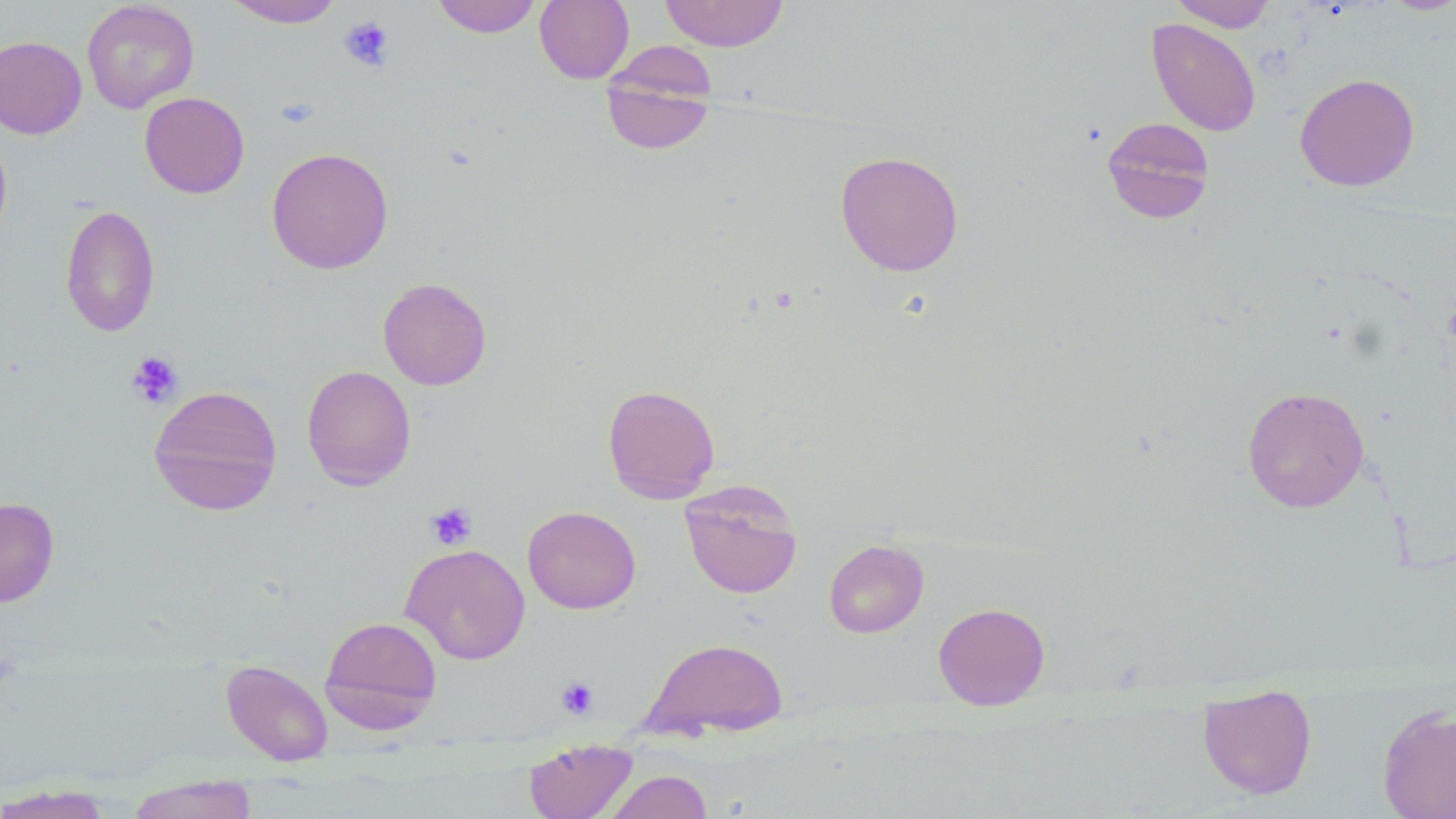
Approximate bounding boxes as (x1, y1, x2, y2) in pixels. Platelet locations: (338, 16, 394, 72), (276, 95, 318, 129), (126, 351, 183, 409), (425, 501, 478, 550), (555, 676, 599, 720). Uninfected red blood cell locations: (225, 0, 345, 28), (431, 0, 543, 38), (535, 0, 635, 84), (659, 0, 790, 52), (1169, 0, 1277, 32), (1379, 0, 1456, 16), (81, 1, 199, 113), (1147, 18, 1261, 137), (0, 36, 87, 139), (600, 42, 718, 155), (1294, 73, 1420, 192), (139, 92, 249, 198), (1101, 116, 1216, 224), (0, 128, 12, 245), (266, 147, 393, 274), (835, 150, 964, 276), (60, 204, 160, 337), (377, 277, 492, 390), (301, 365, 417, 491), (603, 384, 720, 504), (148, 385, 284, 516), (1241, 386, 1369, 513), (679, 481, 803, 599), (0, 497, 59, 608), (522, 505, 641, 614), (823, 539, 929, 638), (400, 543, 530, 664), (933, 602, 1050, 710), (320, 615, 443, 732), (642, 637, 789, 739), (221, 659, 334, 766), (1197, 684, 1317, 800), (1377, 704, 1456, 819), (524, 738, 637, 819), (602, 770, 713, 819), (126, 776, 258, 819), (0, 784, 115, 818). Slide-level diagnosis: no evidence of blood parasites. May-Grünwald-Giemsa-stained preparation. Single field of view. Image is 1456×819 pixels. 1000x magnification. Optical microscopy. Thin blood film.